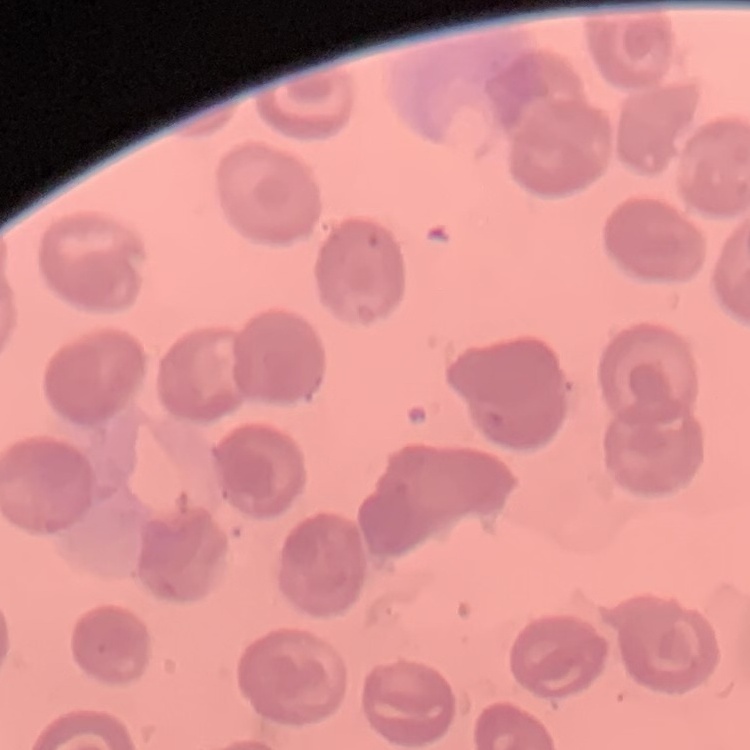 The red blood cells show no rouleaux formation. Field's or Giemsa stain. Thin blood film. One tile cut from a larger photomicrograph.